Report the malaria status of this cell.
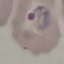
Parasitized.

Photographed with a smartphone camera at the microscope eyepiece. Automatically extracted cell patch, resized to 64 × 64 pixels. Giemsa-stained preparation. Thin blood smear.